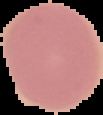
image size = 103×115 pixels
malaria status = uninfected
preparation = thin blood smear
image type = segmented cell region on a black background